State the preparation type.
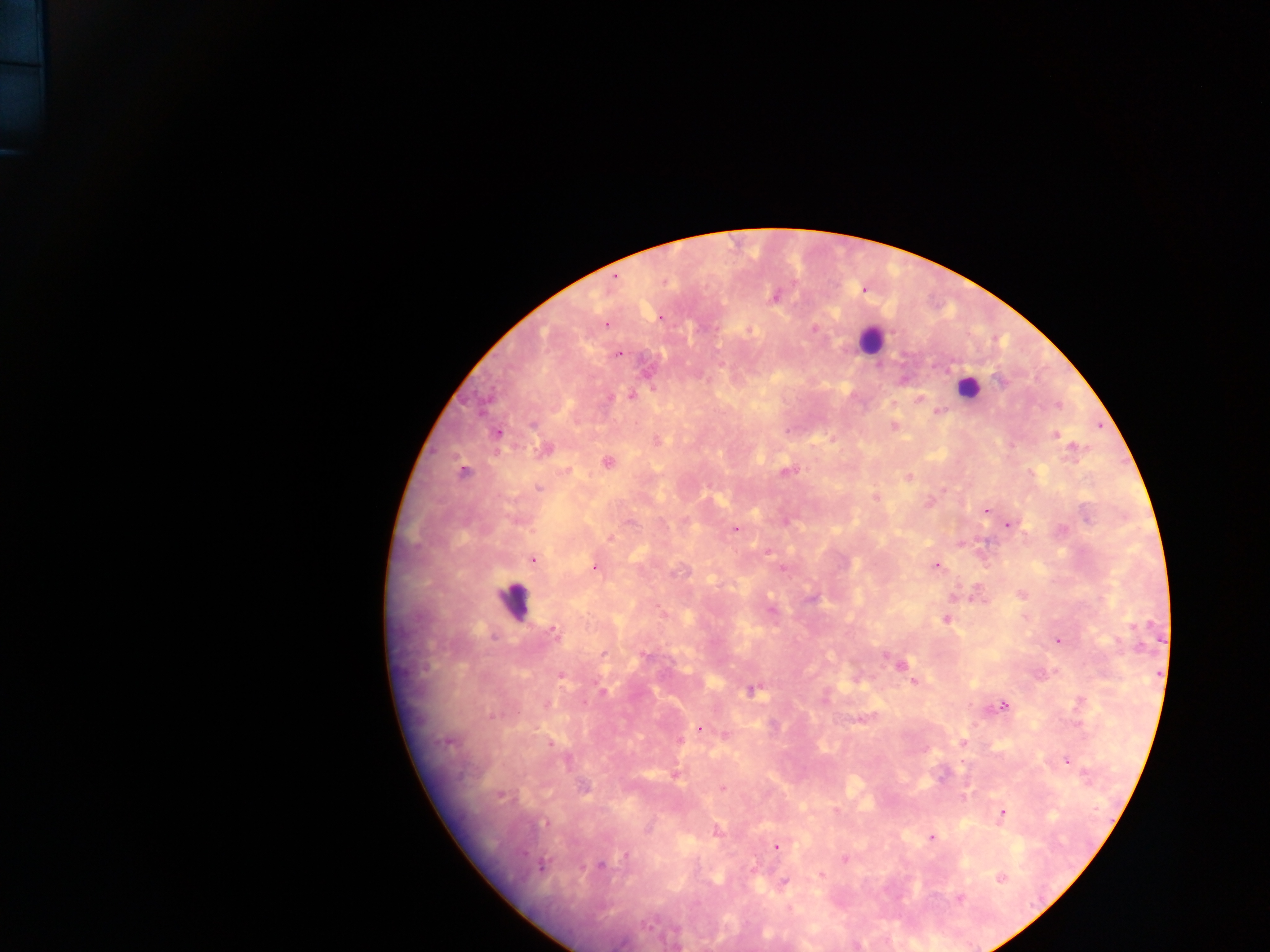
This is a thick smear.

Approximate centers as {x, y} in pixels. Leukocyte locations: {866, 340}, {968, 389}, {514, 610}. Malaria parasite locations: {615, 275}, {665, 281}, {772, 296}, {606, 323}, {815, 328}, {750, 330}, {616, 354}, {1001, 382}, {630, 394}, {916, 399}, {892, 424}, {495, 433}, {1055, 434}, {607, 463}, {785, 469}, {464, 471}, {1030, 473}, {908, 476}, {538, 488}, {876, 497}, {929, 500}, {984, 512}, {628, 522}, {1007, 524}, {734, 529}, {609, 536}, {532, 559}, {936, 565}, {594, 566}, {974, 589}, {1022, 595}, {953, 596}, {946, 619}, {551, 631}, {1057, 641}, {644, 657}, {901, 667}, {559, 676}, {915, 681}, {602, 690}, {750, 690}, {1004, 705}, {701, 727}, {447, 742}, {962, 742}, {1068, 761}, {722, 787}, {501, 795}, {965, 795}, {1004, 814}, {544, 823}, {648, 831}, {716, 831}, {930, 837}, {773, 846}, {621, 858}, {844, 859}, {543, 864}, {600, 865}, {820, 874}, {1000, 877}, {784, 881}, {960, 898}. Mobile-phone photograph taken through the microscope. Image is 1270×952 pixels. Collected in Ghana. One field of view.